Comment on the morphology of the erythrocytes.
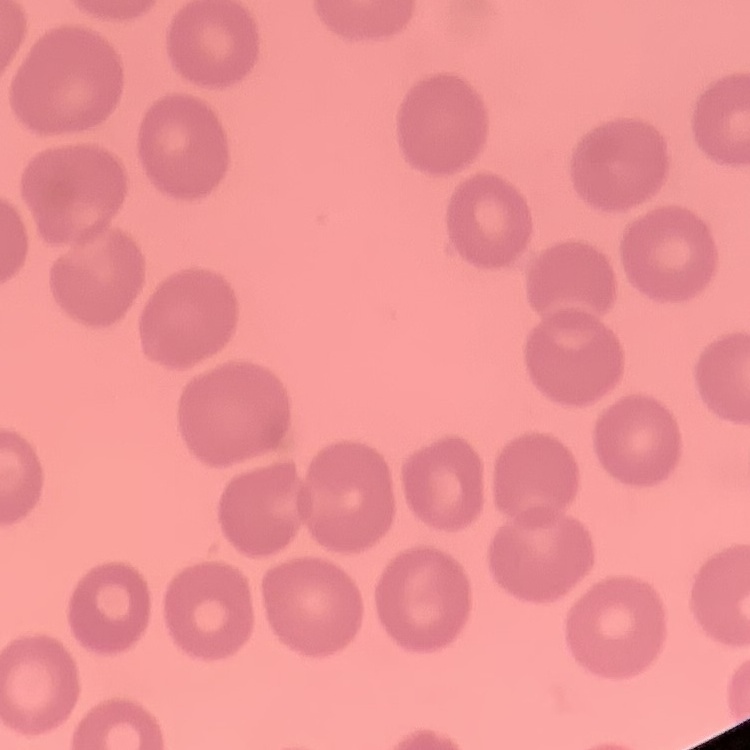
They show no rouleaux formation.

preparation = thin blood smear
stain = Field's or Giemsa
image type = square crop of a larger photomicrograph